State which cell type is depicted.
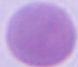
An erythrocyte.

{
  "modality": "micrograph",
  "magnification": "1000x"
}